Classify this cell by malaria status.
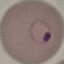
It is parasitized.

Giemsa stain. Automatically extracted cell patch, resized to 64 × 64 pixels. Photographed with a smartphone camera at the microscope eyepiece. Thin blood smear.